Give the position of every Plasmodium parasite visible.
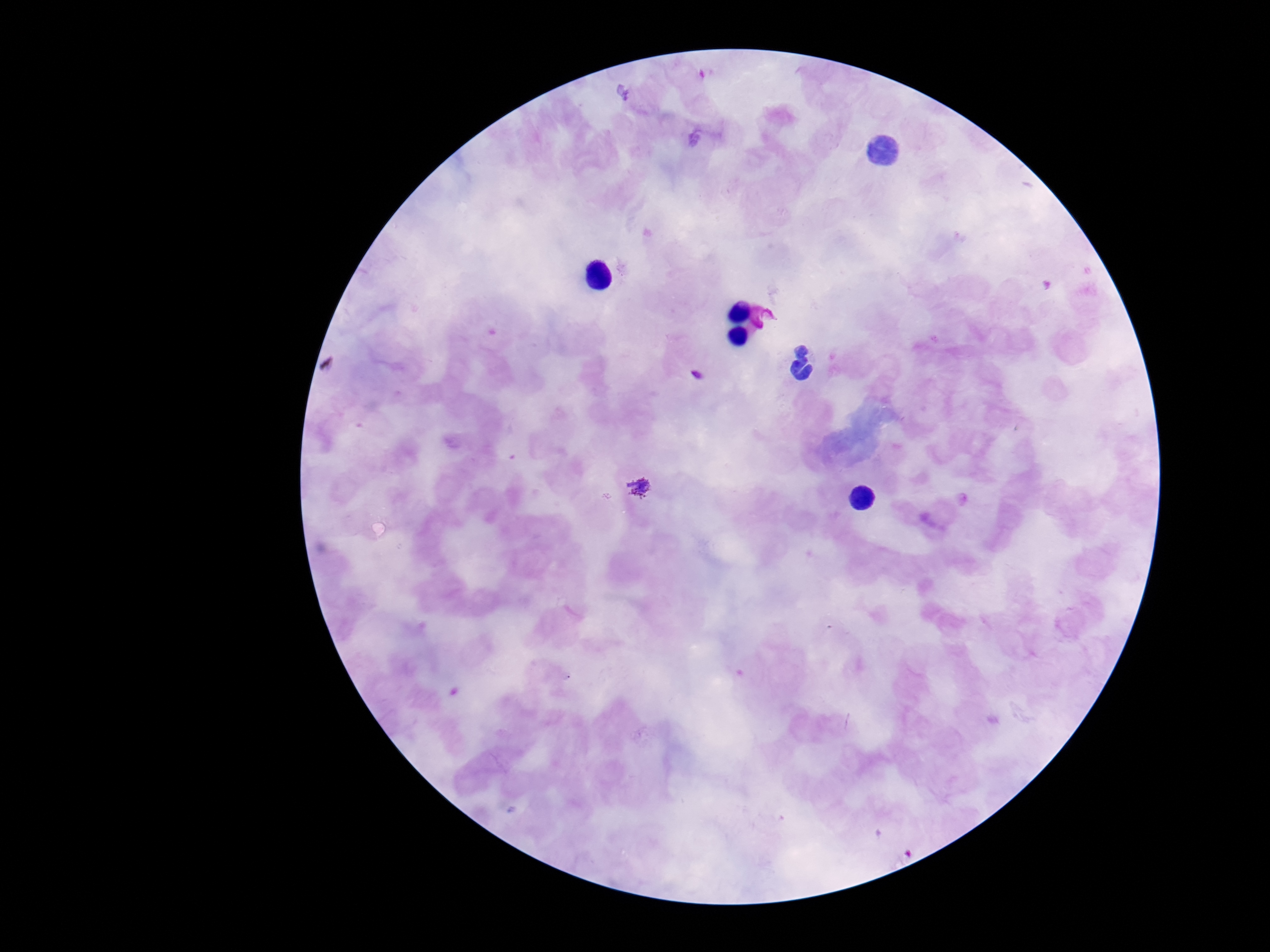

Approximate centers as (x, y) in pixels.
Plasmodium parasites: (697, 375), (642, 488).

preparation: thick blood smear
stain: Giemsa
field_of_view: one from this slide
capture: smartphone camera through the microscope eyepiece
image_size: 1270×952 pixels
magnification: 100x
patient_malaria_status: infected